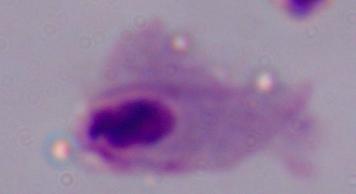

Summary:
  - Identification: trichomonad
  - Magnification: 1000x
  - Modality: photomicrograph